Give the extent of all white blood cells.
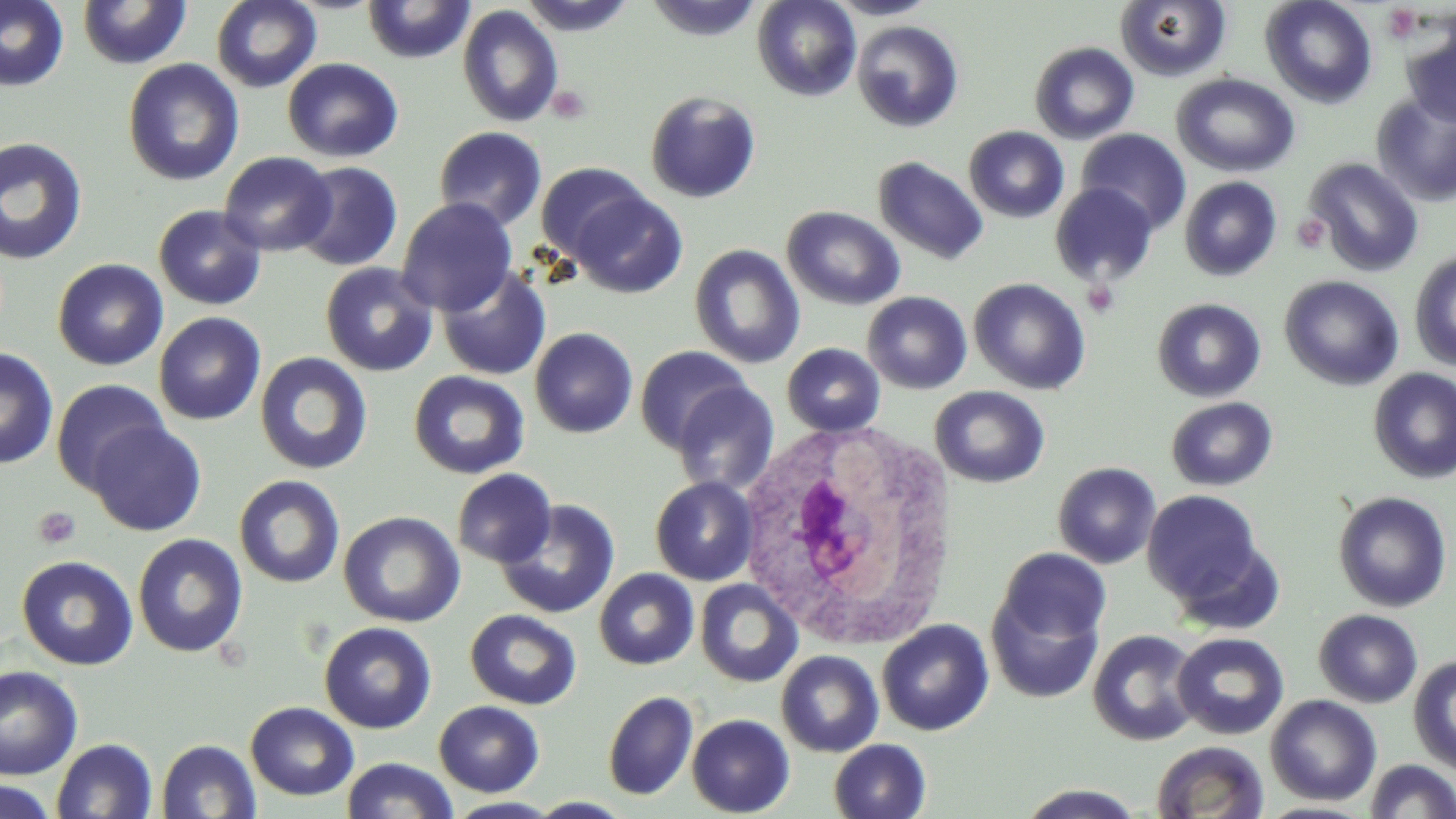

Approximate bounding boxes as (x1,y1)-(x2,y2) corner pairs in pixels.
White blood cells: (736,422)-(964,652).

Summary:
  - Uninfected red blood cell locations: (0,0)-(69,91), (210,0)-(322,92), (361,0)-(476,64), (518,0)-(637,36), (644,0)-(765,42), (751,0)-(862,101), (825,0)-(939,20), (1259,0)-(1378,109), (76,1)-(192,69), (1114,1)-(1232,82), (456,5)-(563,127), (1400,13)-(1456,128), (852,20)-(964,133), (1029,41)-(1140,144), (282,58)-(403,163), (122,59)-(245,186), (1171,73)-(1300,177), (644,90)-(761,203), (1371,92)-(1456,207), (433,126)-(547,231), (964,126)-(1069,223), (1075,129)-(1191,235), (0,137)-(89,266), (218,151)-(336,256), (873,156)-(989,265), (1304,157)-(1424,277), (291,161)-(403,271), (535,161)-(649,263), (1179,176)-(1283,281), (1050,183)-(1159,287), (569,188)-(687,297), (396,197)-(517,316), (153,205)-(266,310), (781,205)-(906,310), (688,244)-(805,369), (1409,251)-(1456,372), (52,258)-(169,371), (320,262)-(439,377), (436,265)-(551,381), (1279,275)-(1405,391), (969,277)-(1091,395), (862,292)-(973,394), (1152,297)-(1266,402), (153,312)-(266,425), (529,327)-(638,438), (782,343)-(885,436), (634,345)-(753,453), (0,347)-(59,470), (255,352)-(373,475), (1368,368)-(1456,484), (408,370)-(530,479), (50,379)-(171,493), (671,383)-(779,496), (929,385)-(1050,488), (1165,396)-(1278,491), (86,420)-(206,536), (1052,462)-(1162,568), (452,469)-(557,568), (233,474)-(345,588), (650,476)-(758,586), (1142,489)-(1266,606), (1332,491)-(1453,613), (495,499)-(620,619), (338,510)-(464,627), (132,533)-(248,658), (996,547)-(1111,646), (16,555)-(138,670), (594,568)-(699,670), (694,579)-(802,688), (986,586)-(1105,705), (465,609)-(581,710), (1314,609)-(1423,708), (877,619)-(993,736), (318,622)-(437,734), (1087,629)-(1202,746), (1172,632)-(1289,740), (776,651)-(884,757), (1408,655)-(1456,774), (0,665)-(83,781), (603,690)-(699,801), (1265,695)-(1382,806), (433,700)-(544,797), (245,701)-(359,802), (686,714)-(795,817), (52,738)-(158,819), (155,739)-(261,819), (828,739)-(931,819), (1150,740)-(1270,819), (341,756)-(459,818), (1364,759)-(1456,819), (0,778)-(59,819), (1015,783)-(1150,818), (526,796)-(636,817), (444,797)-(564,817)
  - Platelet locations: (1382,4)-(1422,43), (546,85)-(591,123), (1292,214)-(1330,253), (33,506)-(81,549)
  - Slide-level diagnosis: no evidence of blood parasites
  - Field of view: single
  - Modality: optical microscopy
  - Stain: May-Grünwald-Giemsa
  - Magnification: 1000x
  - Image size: 1456×819 pixels
  - Preparation: thin blood film